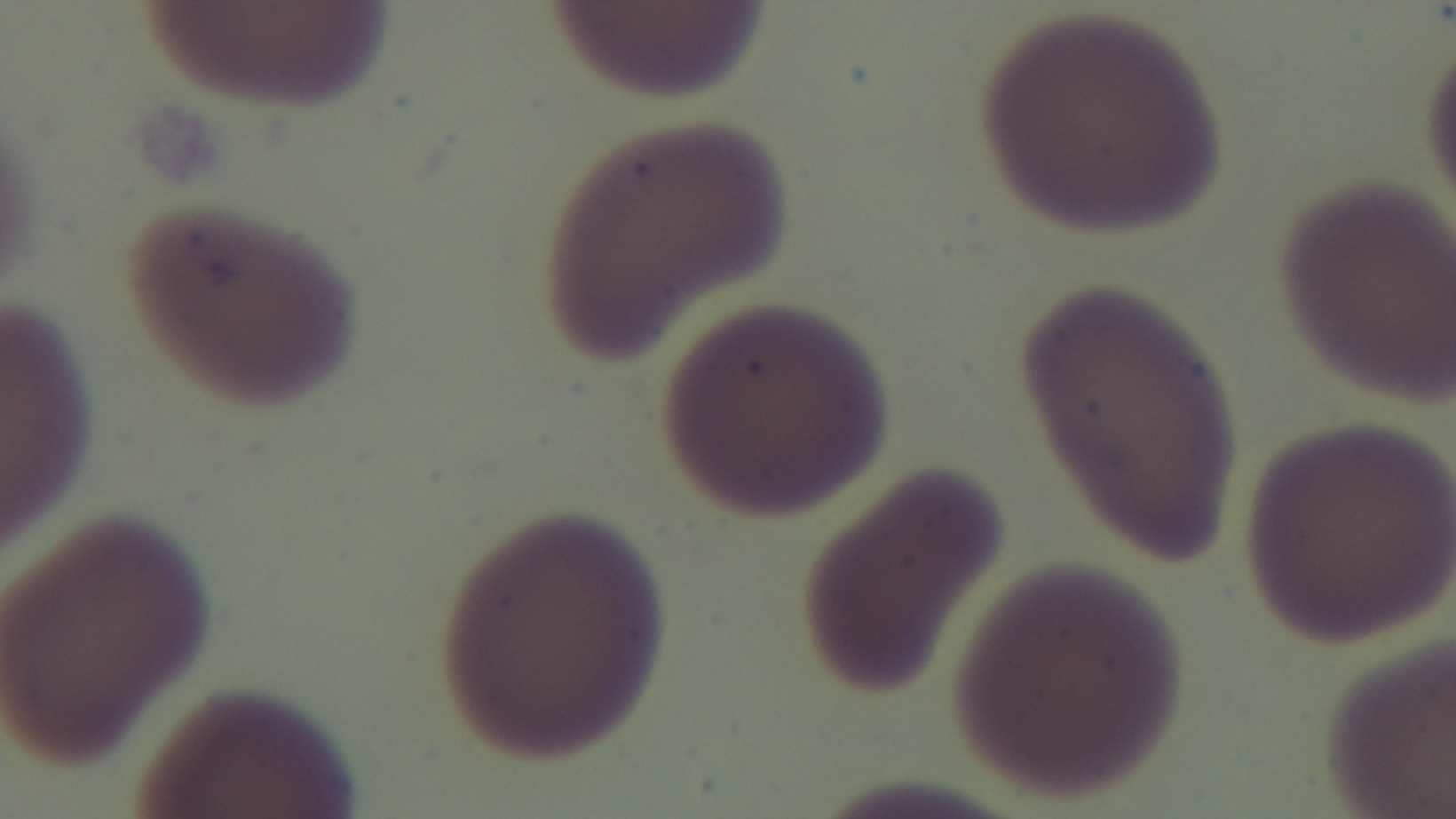 Malaria status: uninfected. Oil-immersion objective, 100x. Preparation: thin smear. Single field of view. Giemsa-stained. Mounted 4K digital camera. Photomicrograph.